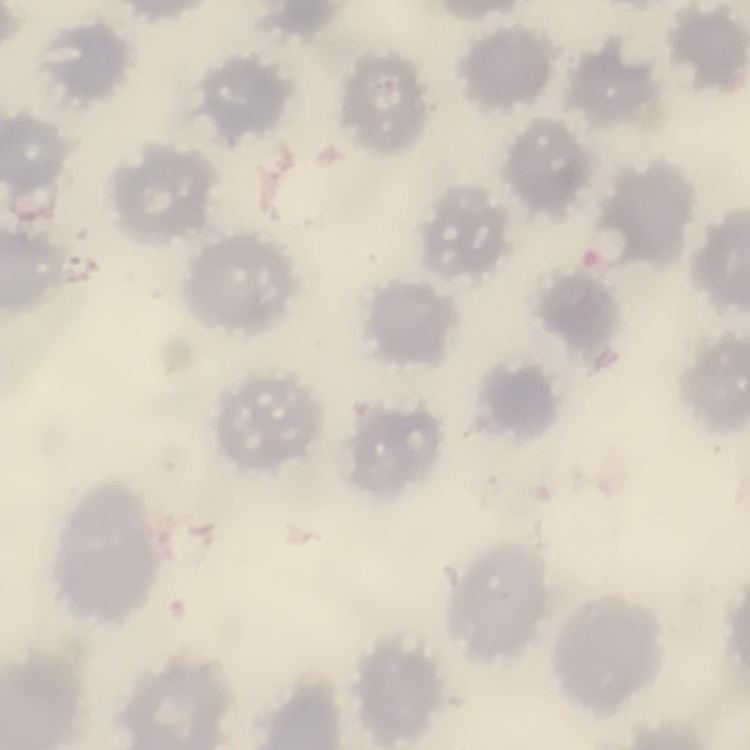

red blood cell morphology = no rouleaux formation
image type = one tile cut from a larger photomicrograph
preparation = thin blood film
stain = Field's or Giemsa